Give the position of every Plasmodium parasite.
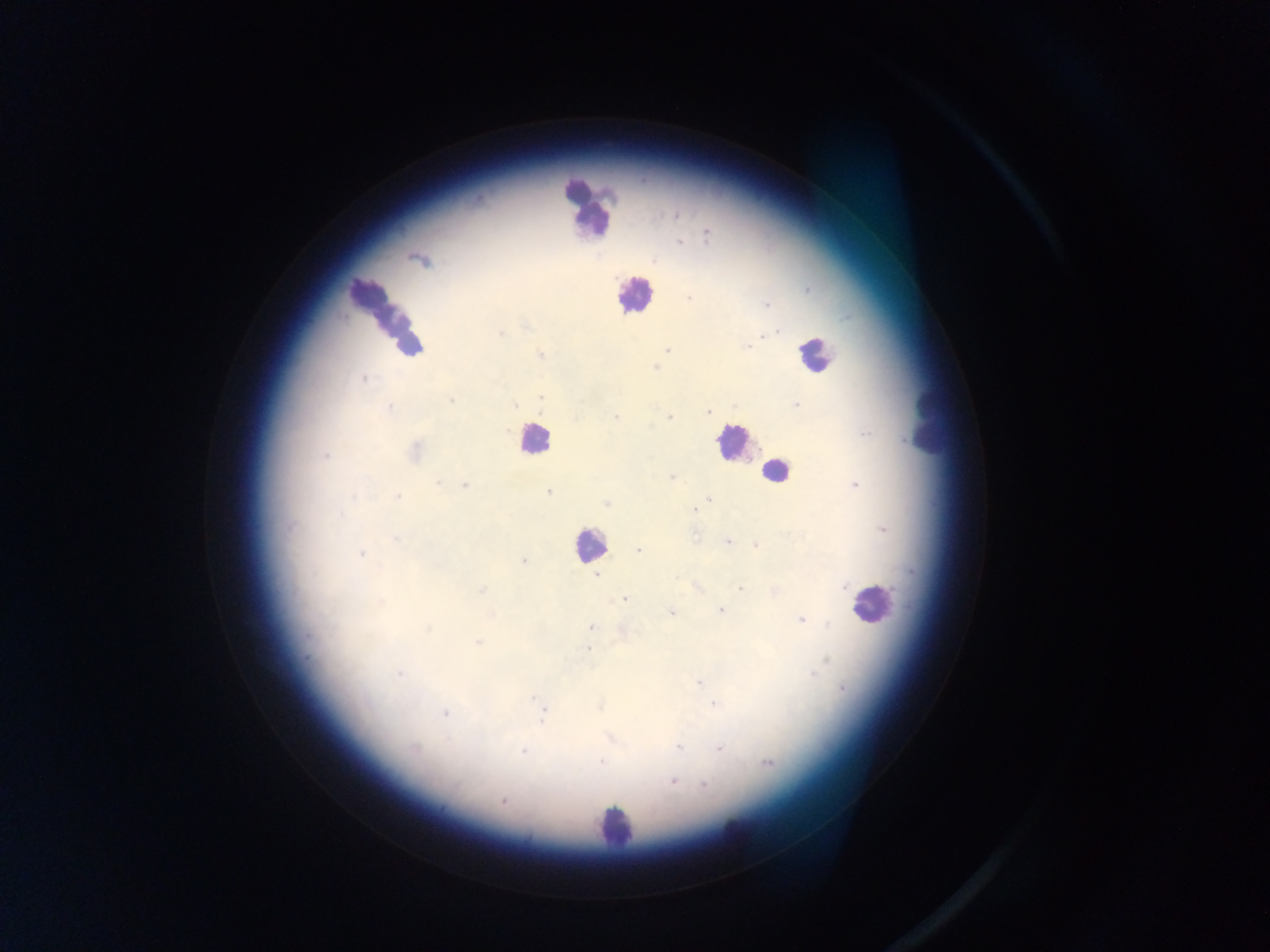
Approximate centers as (x, y) in pixels.
Plasmodium parasites: (478, 199), (677, 215), (706, 234), (679, 242), (652, 261), (689, 299), (767, 304), (771, 333), (500, 334), (746, 347), (668, 350), (541, 354), (655, 366), (363, 379), (540, 397), (451, 401), (795, 405), (515, 406), (389, 407), (708, 412), (669, 417), (616, 418), (414, 452), (325, 456), (672, 478), (438, 482), (465, 484), (855, 485), (548, 492), (398, 497), (708, 500), (607, 504), (695, 508), (290, 526), (395, 539), (728, 541), (757, 545), (638, 549), (360, 554), (523, 561), (597, 576), (844, 587), (740, 588), (481, 590), (625, 600), (379, 603), (721, 611), (671, 612), (801, 620), (590, 627), (428, 628), (308, 636), (477, 643), (589, 649), (399, 674), (813, 674), (699, 683), (843, 688), (534, 698), (714, 704), (599, 707), (445, 714), (542, 719), (678, 747), (720, 748), (413, 749), (523, 752), (602, 761), (769, 764), (672, 782), (705, 785), (502, 801).

Summary:
  - Leukocyte locations: (588, 207), (634, 295), (386, 316), (813, 354), (926, 415), (533, 440), (735, 444), (777, 471), (588, 544), (870, 604), (612, 826), (738, 845)
  - Capture: mobile-phone photograph through a microscope
  - Country: Ghana
  - Field of view: single
  - Preparation: thick blood film
  - Image size: 1270×952 pixels